Assess this cell for malaria.
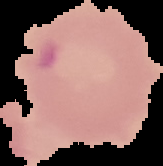

It is parasitized.

{
  "image_type": "segmented cell region on a black background",
  "preparation": "thin blood film",
  "image_size": "163×166 pixels"
}